Outline each blood parasite and name the species.
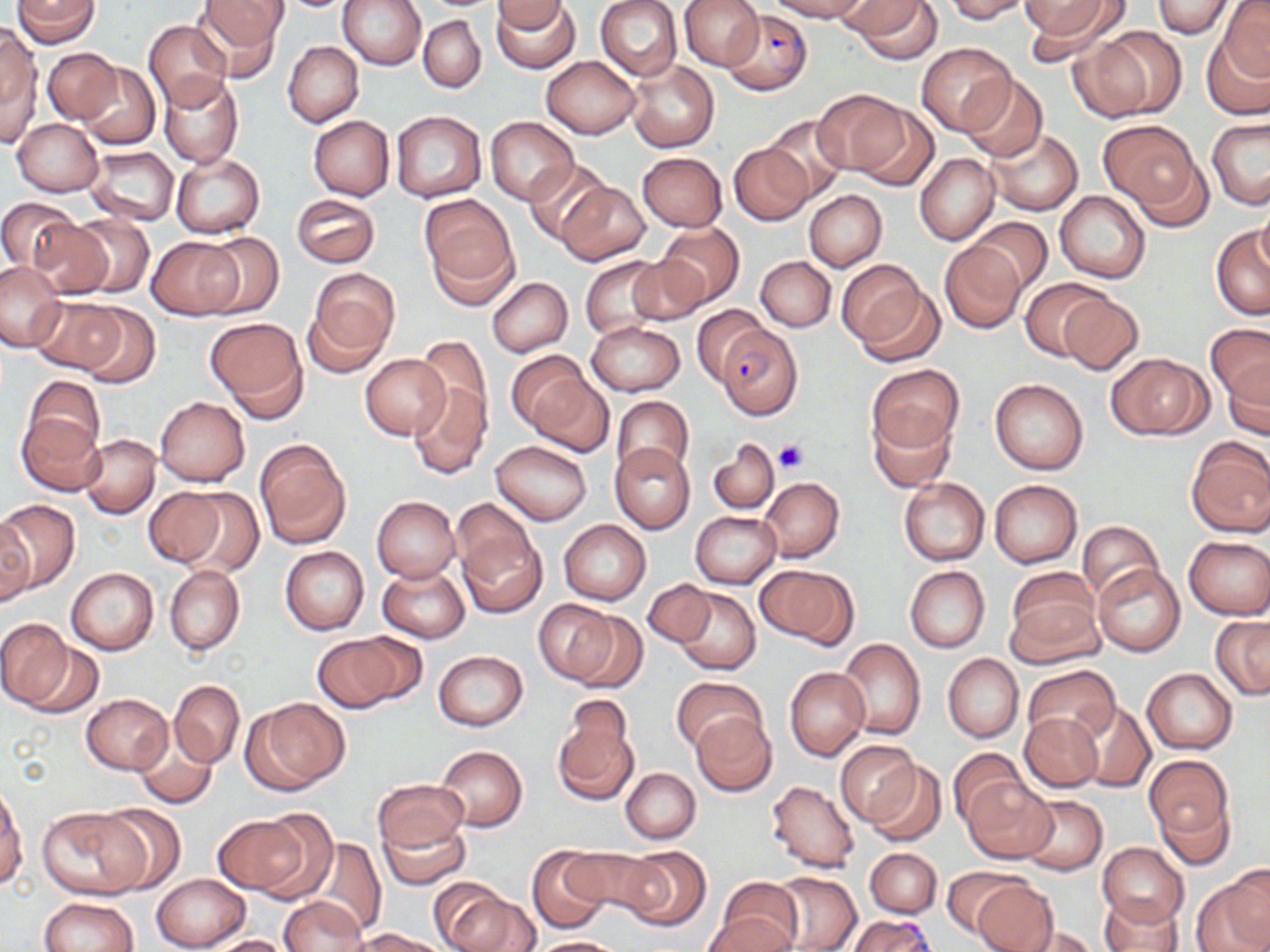
Approximate bounding boxes as [x1, y1, x2, y2] in pixels.
Plasmodium falciparum-infected red blood cells: [723, 9, 810, 95], [716, 325, 804, 421], [847, 918, 937, 951].
No Plasmodium ovale, Plasmodium malariae, Plasmodium vivax, Babesia divergens, or Trypanosoma brucei observed.

Summary:
  - Uninfected red blood cell locations: [11, 0, 100, 47], [339, 0, 425, 70], [595, 0, 682, 80], [678, 0, 763, 71], [765, 0, 871, 22], [843, 0, 944, 62], [943, 0, 1030, 23], [1023, 0, 1121, 46], [1152, 0, 1234, 39], [492, 1, 572, 33], [493, 1, 581, 73], [1217, 1, 1270, 81], [193, 2, 287, 78], [609, 3, 696, 147], [653, 3, 746, 117], [419, 14, 486, 92], [144, 19, 233, 110], [0, 27, 41, 144], [1090, 27, 1186, 120], [1203, 33, 1270, 121], [283, 41, 363, 127], [916, 42, 1016, 135], [43, 47, 120, 125], [541, 56, 638, 139], [626, 60, 719, 153], [76, 62, 160, 149], [159, 73, 244, 168], [959, 76, 1047, 162], [815, 90, 907, 172], [849, 103, 939, 191], [390, 111, 487, 202], [309, 115, 394, 200], [761, 115, 851, 202], [485, 117, 578, 206], [13, 118, 103, 196], [1207, 118, 1270, 209], [1100, 120, 1202, 211], [984, 126, 1082, 215], [727, 143, 811, 226], [84, 146, 179, 226], [637, 152, 727, 230], [170, 153, 266, 237], [914, 154, 999, 246], [525, 158, 611, 245], [556, 180, 649, 265], [1054, 190, 1151, 283], [804, 191, 887, 271], [290, 193, 380, 268], [419, 196, 518, 302], [0, 198, 79, 271], [1257, 199, 1270, 274], [63, 213, 154, 297], [969, 218, 1052, 295], [25, 219, 113, 300], [655, 222, 744, 306], [1211, 228, 1269, 320], [198, 231, 284, 317], [147, 237, 239, 320], [940, 241, 1026, 333], [626, 255, 710, 326], [579, 256, 666, 340], [756, 256, 836, 331], [837, 259, 933, 350], [0, 261, 63, 351], [305, 270, 399, 375], [487, 277, 573, 356], [1020, 278, 1111, 360], [1058, 293, 1143, 375], [29, 296, 133, 375], [77, 302, 161, 388], [691, 305, 769, 386], [206, 317, 308, 418], [587, 320, 684, 397], [1205, 323, 1270, 404], [413, 338, 493, 433], [361, 353, 451, 438], [1108, 353, 1210, 440], [510, 354, 605, 448], [1223, 357, 1270, 438], [866, 364, 964, 454], [22, 374, 105, 459], [989, 377, 1089, 475], [407, 381, 492, 479], [611, 395, 693, 478], [155, 397, 249, 485], [868, 410, 956, 491], [17, 414, 105, 497], [80, 434, 161, 518], [1185, 436, 1270, 537], [255, 439, 350, 548], [708, 439, 780, 514], [491, 440, 592, 525], [609, 441, 696, 534], [898, 477, 989, 565], [759, 478, 844, 562], [989, 480, 1081, 568], [143, 487, 229, 568], [173, 488, 264, 576], [372, 495, 460, 582], [450, 498, 536, 583], [0, 500, 81, 594], [690, 511, 781, 588], [0, 514, 35, 608], [560, 520, 650, 604], [1076, 520, 1162, 604], [458, 530, 548, 618], [1184, 535, 1270, 619], [280, 546, 368, 635], [757, 562, 857, 648], [1092, 564, 1186, 657], [163, 565, 244, 656], [905, 565, 990, 652], [378, 566, 470, 642], [67, 567, 159, 655], [1008, 567, 1099, 653], [1008, 574, 1105, 735], [643, 578, 716, 648], [670, 585, 761, 675], [535, 599, 621, 683], [569, 612, 648, 694], [1211, 616, 1270, 701], [0, 619, 73, 709], [313, 631, 419, 712], [837, 638, 926, 740], [20, 642, 105, 719], [434, 650, 527, 731], [943, 654, 1024, 741], [1024, 665, 1120, 749], [784, 667, 869, 760], [1142, 668, 1238, 754], [670, 675, 764, 753], [170, 680, 244, 768], [81, 693, 173, 775], [245, 697, 349, 794], [1072, 701, 1155, 792], [552, 712, 639, 807], [690, 712, 777, 798], [1020, 713, 1102, 792], [131, 730, 219, 809], [835, 740, 920, 827], [436, 745, 527, 832], [949, 749, 1026, 826], [1145, 755, 1231, 842], [863, 759, 946, 846], [621, 768, 700, 843], [964, 775, 1058, 864], [373, 779, 468, 855], [765, 779, 860, 872], [0, 785, 26, 889], [1016, 793, 1108, 875], [1154, 794, 1236, 870], [95, 805, 186, 895], [37, 807, 145, 900], [245, 809, 339, 904], [378, 814, 470, 891], [213, 815, 309, 896], [300, 835, 386, 936], [1096, 843, 1189, 927], [527, 846, 611, 933], [564, 846, 663, 920], [620, 846, 710, 932], [868, 849, 940, 920], [941, 866, 1023, 937], [769, 871, 860, 952], [1192, 871, 1270, 952], [150, 872, 249, 951], [715, 877, 803, 949], [970, 879, 1059, 952], [432, 882, 532, 952], [1098, 894, 1184, 952], [280, 896, 369, 952], [40, 897, 139, 952], [702, 914, 796, 952], [1009, 927, 1102, 951], [356, 929, 450, 952], [199, 934, 297, 952], [529, 937, 626, 952]
  - Platelet locations: [773, 438, 808, 473]
  - Slide-level diagnosis: Plasmodium falciparum
  - Stain: May-Grünwald-Giemsa
  - Field of view: single
  - Image size: 1270×952 pixels
  - Magnification: 1000x
  - Modality: light microscopy
  - Preparation: thin blood film